Report the malaria status of this cell.
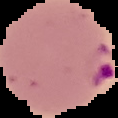

Parasitized.

Segmented cell region on a black background. Image is 118×118 pixels. From a thin blood smear.